State the preparation type.
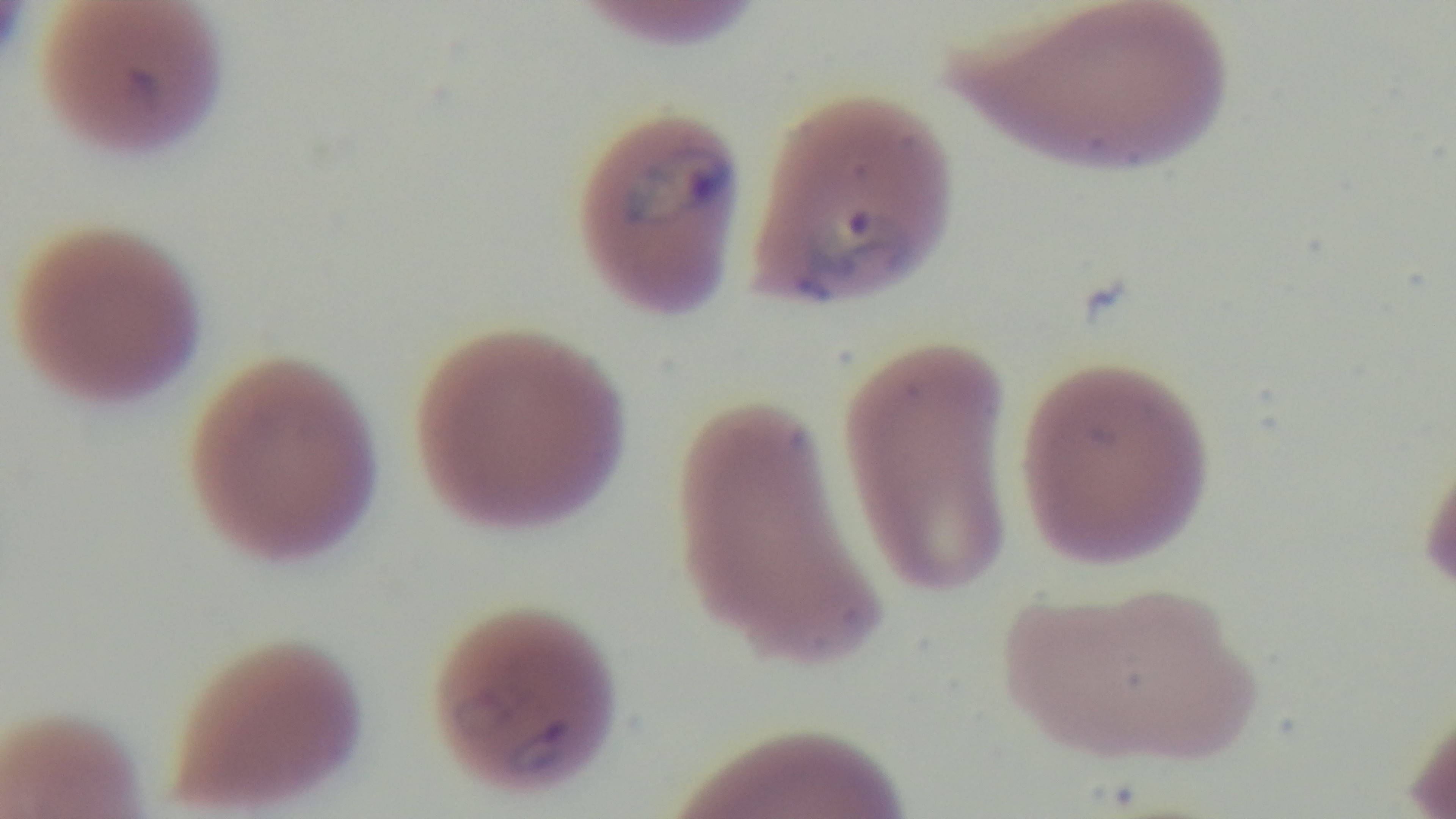
Thin.

objective = 100x oil immersion
field of view = single
malaria status = positive
stain = Giemsa
capture = mounted 4K digital camera
modality = light microscopy